Identify the parasite.
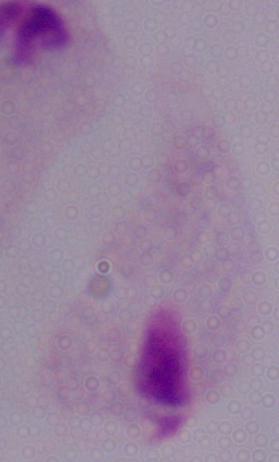
A trichomonad.

modality = photomicrograph
magnification = 1000x